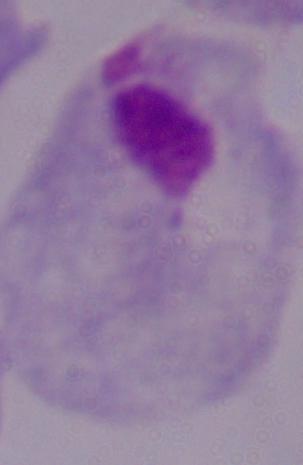
magnification = 1000x
modality = photomicrograph
identification = trichomonad